Identify the parasite.
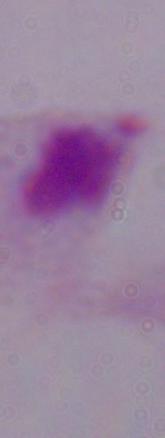
This is a trichomonad.

modality = micrograph
magnification = 1000x